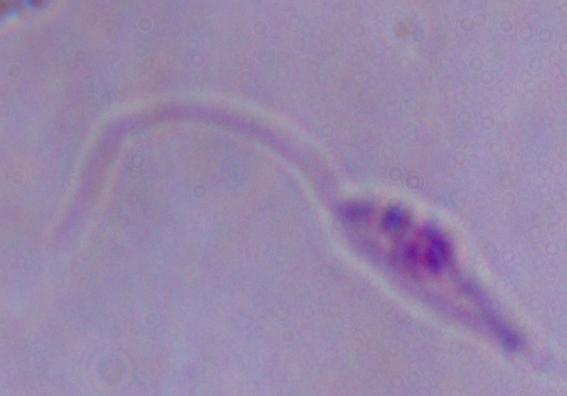
magnification = 1000x
modality = micrograph
identification = Leishmania